Draw a bounding box around every leukocyte (white blood cell).
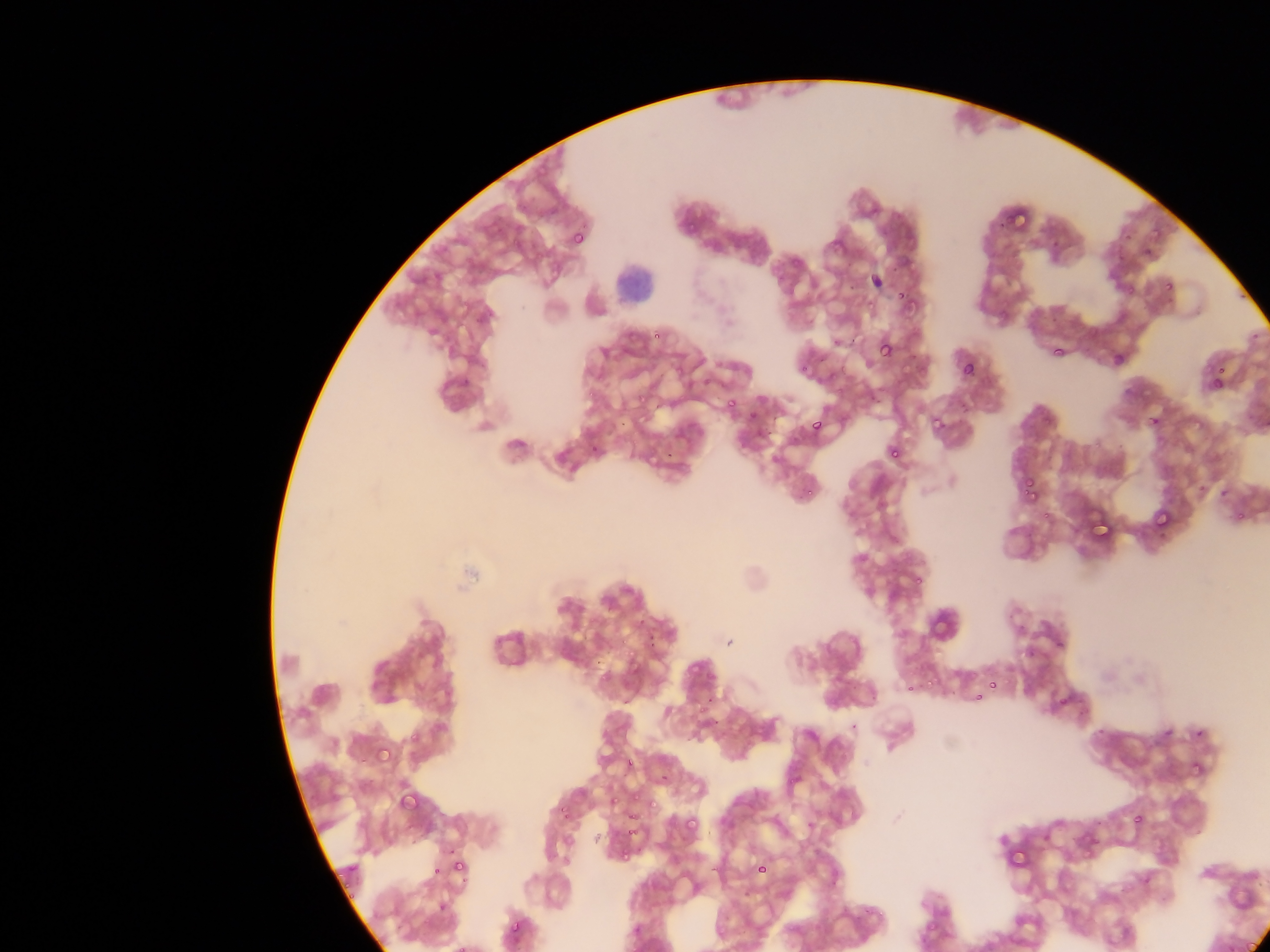
Approximate bounding boxes as {left, top, right, bottom} in pixels.
Leukocytes: {616, 260, 651, 311}.

Malaria parasite locations: {1004, 201, 1039, 236}, {685, 221, 699, 235}, {572, 228, 589, 247}, {1164, 280, 1175, 292}, {895, 290, 905, 300}, {647, 328, 669, 354}, {878, 339, 894, 359}, {1050, 344, 1065, 359}, {960, 361, 975, 377}, {1213, 365, 1226, 380}, {1210, 376, 1224, 390}, {634, 383, 658, 415}, {726, 399, 737, 410}, {931, 407, 958, 434}, {746, 409, 757, 421}, {1149, 414, 1162, 428}, {810, 420, 822, 432}, {888, 446, 902, 460}, {665, 449, 674, 458}, {1021, 482, 1039, 501}, {804, 487, 817, 498}, {1087, 505, 1113, 537}, {1154, 509, 1173, 529}, {911, 573, 924, 588}, {624, 636, 643, 664}, {1054, 640, 1065, 651}, {1027, 649, 1037, 658}, {988, 680, 997, 689}, {981, 682, 994, 692}, {905, 683, 914, 692}, {973, 693, 983, 702}, {701, 695, 714, 708}, {1053, 697, 1065, 710}, {1194, 728, 1205, 738}, {409, 730, 422, 744}, {378, 748, 394, 764}, {624, 758, 634, 769}, {626, 787, 646, 799}, {648, 790, 664, 810}, {399, 791, 419, 809}, {609, 791, 628, 809}, {558, 805, 569, 816}, {627, 809, 639, 822}, {1133, 814, 1144, 825}, {683, 816, 699, 833}, {615, 848, 632, 871}, {1012, 849, 1035, 872}, {452, 859, 466, 873}, {754, 859, 769, 877}, {432, 865, 442, 876}, {437, 902, 448, 913}, {505, 918, 526, 939}. Sample from Ghana. Mobile-phone photograph taken through the microscope. One field of view. Thin blood smear. Image is 1270×952 pixels.